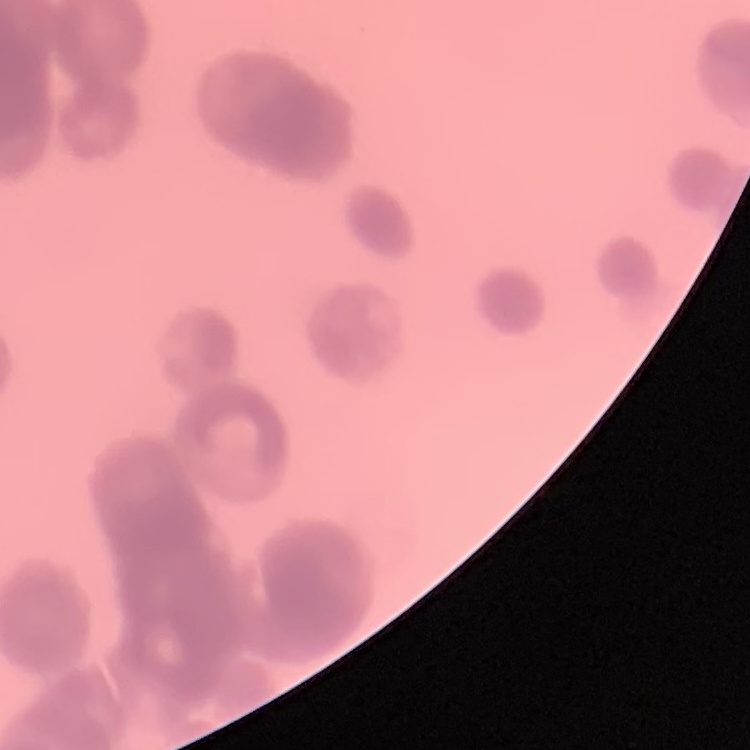
The red blood cells exhibit rouleaux formation. Stained with either Field's or Giemsa. One tile cut from a larger photomicrograph. Thin blood film.